State the blood parasite species.
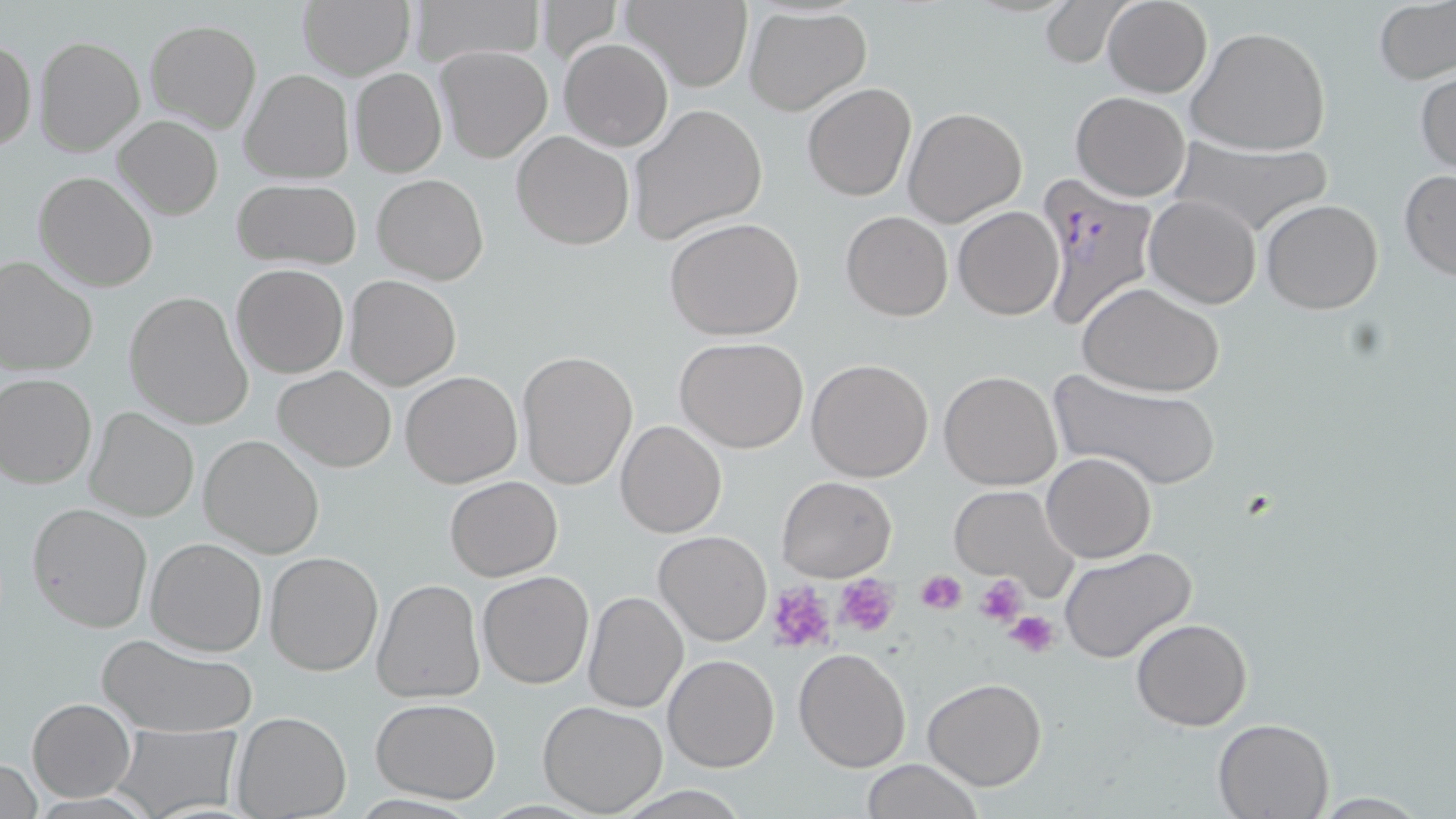

Plasmodium falciparum.

preparation: thin blood smear
platelet_locations: 'approximate bounding boxes as (x1,y1)-(x2,y2) corner pairs in pixels: (915,569)-(968,615), (974,572)-(1028,627), (835,574)-(898,636), (766,581)-(835,653), (1005,609)-(1059,659)'
modality: optical microscopy
magnification: 1000x
field_of_view: single
uninfected_red_blood_cell_locations: 'approximate bounding boxes as (x1,y1)-(x2,y2) corner pairs in pixels: (402,0)-(545,68), (619,0)-(752,92), (1101,0)-(1213,98), (1040,1)-(1129,68), (1375,1)-(1454,85), (297,2)-(413,80), (745,6)-(872,114), (144,19)-(261,133), (1186,24)-(1333,157), (32,35)-(145,157), (559,38)-(672,151), (0,39)-(36,151), (435,45)-(552,162), (239,68)-(355,184), (350,68)-(447,178), (1415,70)-(1456,179), (803,83)-(916,201), (1071,92)-(1190,202), (628,104)-(769,244), (902,106)-(1027,228), (113,115)-(223,220), (512,131)-(635,250), (1163,136)-(1336,237), (1398,170)-(1456,282), (34,171)-(157,291), (373,173)-(489,286), (232,179)-(362,269), (1145,195)-(1261,308), (1261,199)-(1383,313), (953,206)-(1064,321), (840,211)-(953,320), (664,217)-(806,339), (0,257)-(98,376), (230,263)-(348,379), (345,274)-(460,391), (1079,283)-(1226,397), (124,290)-(255,431), (675,337)-(809,454), (516,350)-(637,490), (806,358)-(933,482), (272,365)-(397,472), (939,370)-(1062,491), (1047,370)-(1222,491), (400,371)-(523,489), (0,372)-(98,488), (83,406)-(197,524), (615,421)-(725,538), (197,435)-(325,557), (1042,452)-(1155,563), (445,476)-(562,581), (773,476)-(894,583), (949,486)-(1080,596), (27,501)-(154,632), (653,531)-(772,647), (145,537)-(268,656), (1058,546)-(1199,665), (264,550)-(384,676), (478,570)-(596,691), (374,579)-(484,702), (582,590)-(689,712), (1131,617)-(1253,731), (97,634)-(257,739), (794,647)-(911,772), (663,654)-(781,772), (922,677)-(1048,791), (26,697)-(135,802), (371,698)-(502,803), (537,700)-(668,817), (232,712)-(350,819), (1211,718)-(1335,818), (111,725)-(241,817), (1,758)-(42,818), (861,759)-(985,818), (1306,793)-(1440,817)'
image_size: 1456×819 pixels
plasmodium_falciparum_infected_red_blood_cell_locations: 'approximate bounding boxes as (x1,y1)-(x2,y2) corner pairs in pixels: (1036,177)-(1164,332)'
stain: May-Grünwald-Giemsa